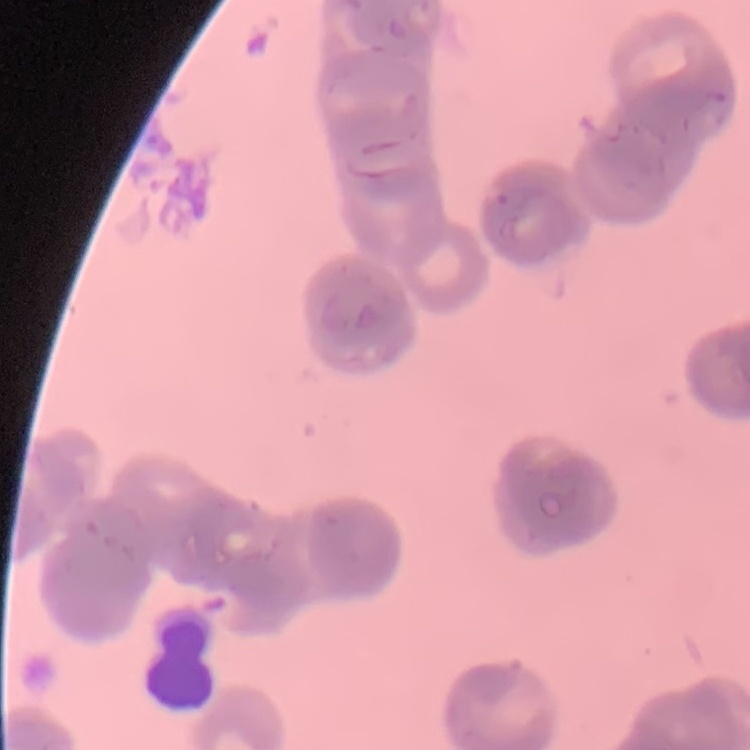

Summary:
  - Erythrocyte morphology: rouleaux formation
  - Stain: Field's or Giemsa
  - Image type: square crop of a larger photomicrograph
  - Preparation: thin blood smear